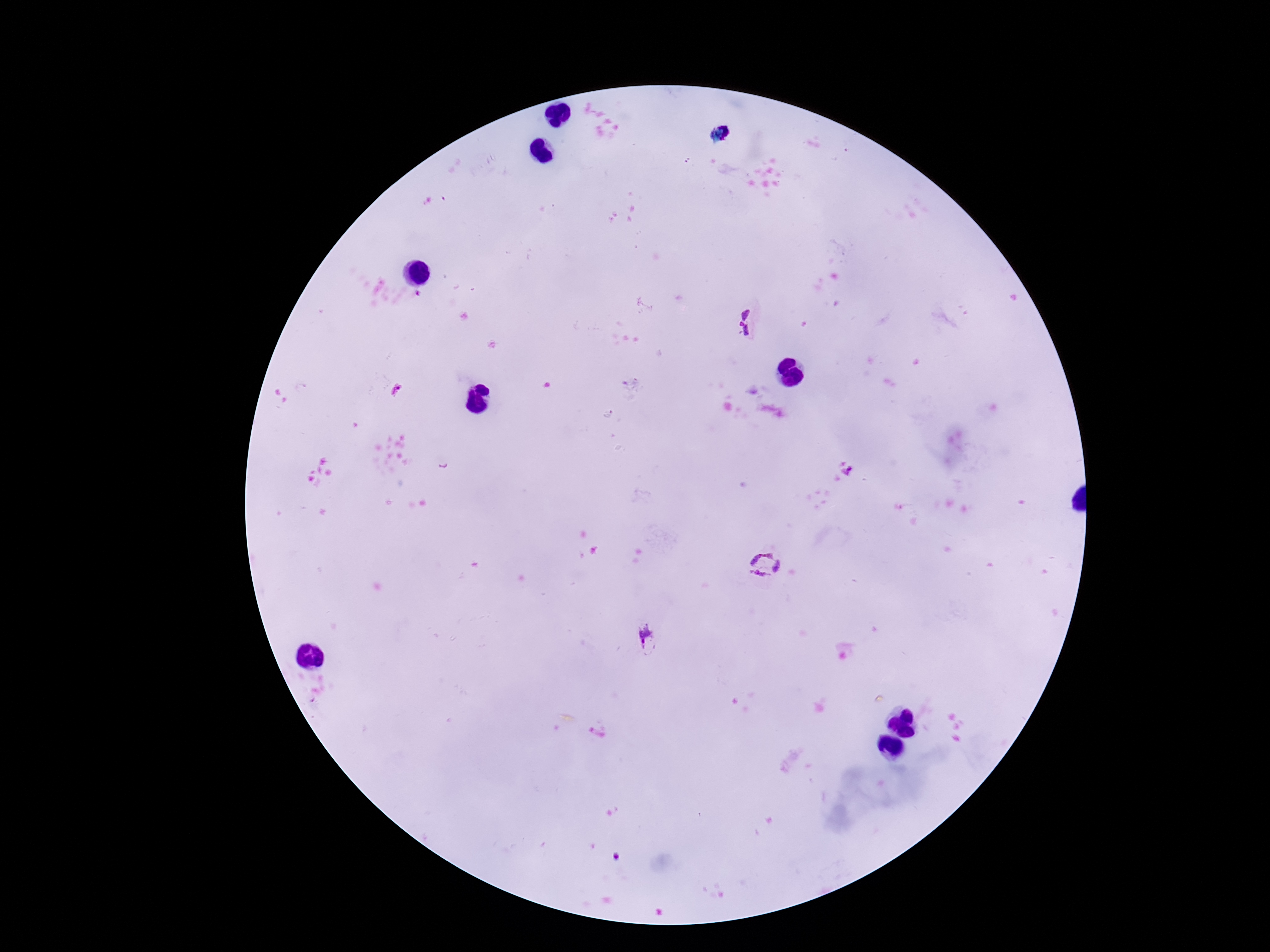
preparation = thick blood smear
stain = Giemsa
field of view = one from this slide
image size = 1270×952 pixels
patient malaria status = infected
Plasmodium parasite locations = approximate centers as {x, y} in pixels: {748, 319}, {849, 471}, {765, 565}, {648, 641}
capture = smartphone camera through the microscope eyepiece
magnification = 100x